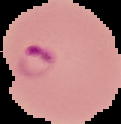
Summary:
  - Image type: segmented cell region with the area outside set to black
  - Preparation: thin blood film
  - Image size: 121×124 pixels
  - Malaria status: parasitized